Comment on the morphology of the erythrocytes.
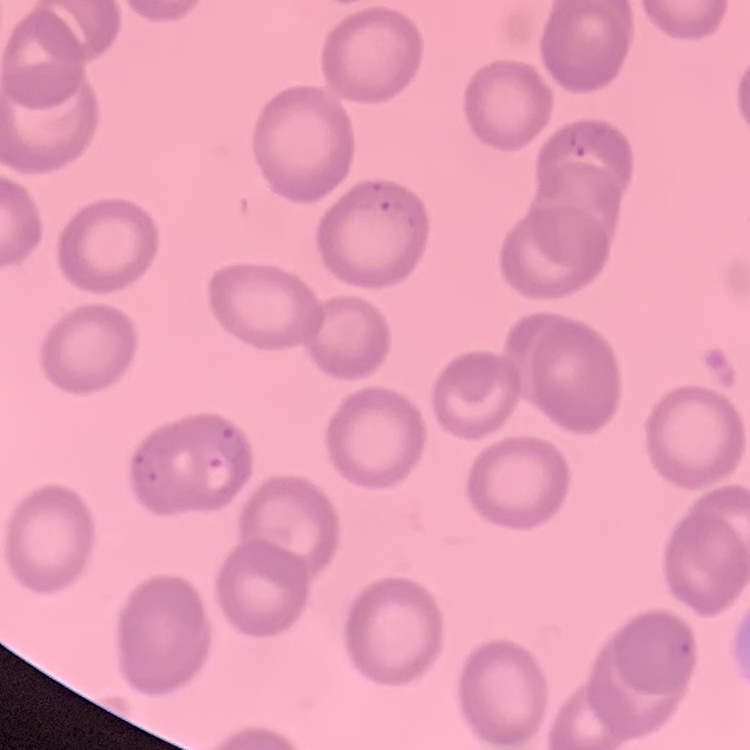

No rouleaux formation.

One tile cut from a larger photomicrograph. Field's or Giemsa stain. Thin blood film.